Comment on the morphology of the erythrocytes.
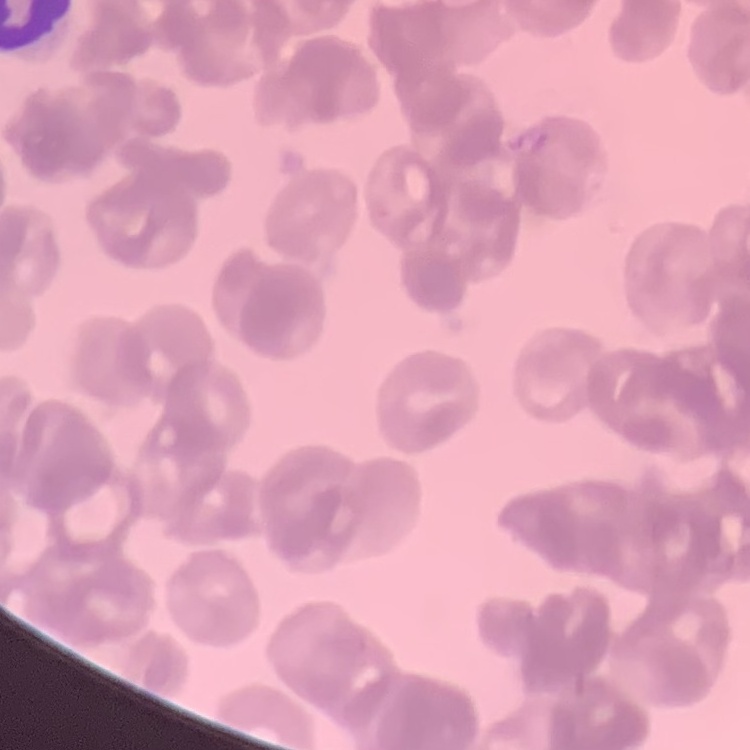
They show rouleaux formation.

preparation = thin blood film
image type = square crop of a larger photomicrograph
stain = Field's or Giemsa